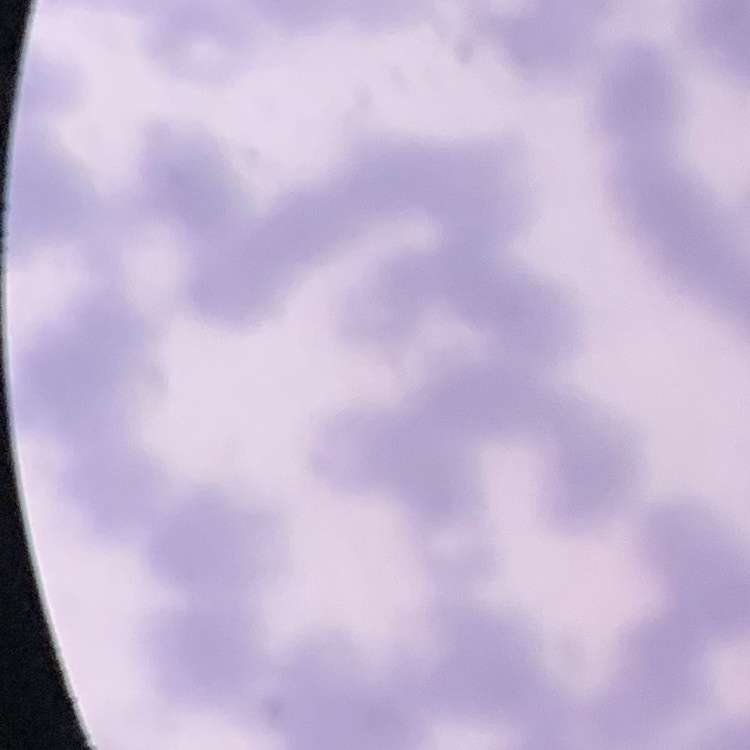 The red blood cells show rouleaux formation. Thin blood film. Field's or Giemsa stain. Square crop of a larger photomicrograph.